Report the malaria status of this cell.
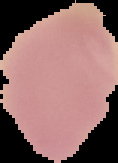

It is uninfected.

preparation: thin blood smear
image_size: 118×163 pixels
image_type: segmented cell region on a black background